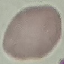

{
  "malaria_status": "uninfected",
  "capture": "smartphone camera at the microscope eyepiece",
  "preparation": "thin smear",
  "image_type": "cell patch, automatically extracted from a larger field of view and resized to 64 × 64 pixels",
  "stain": "Giemsa"
}